Point out cells.
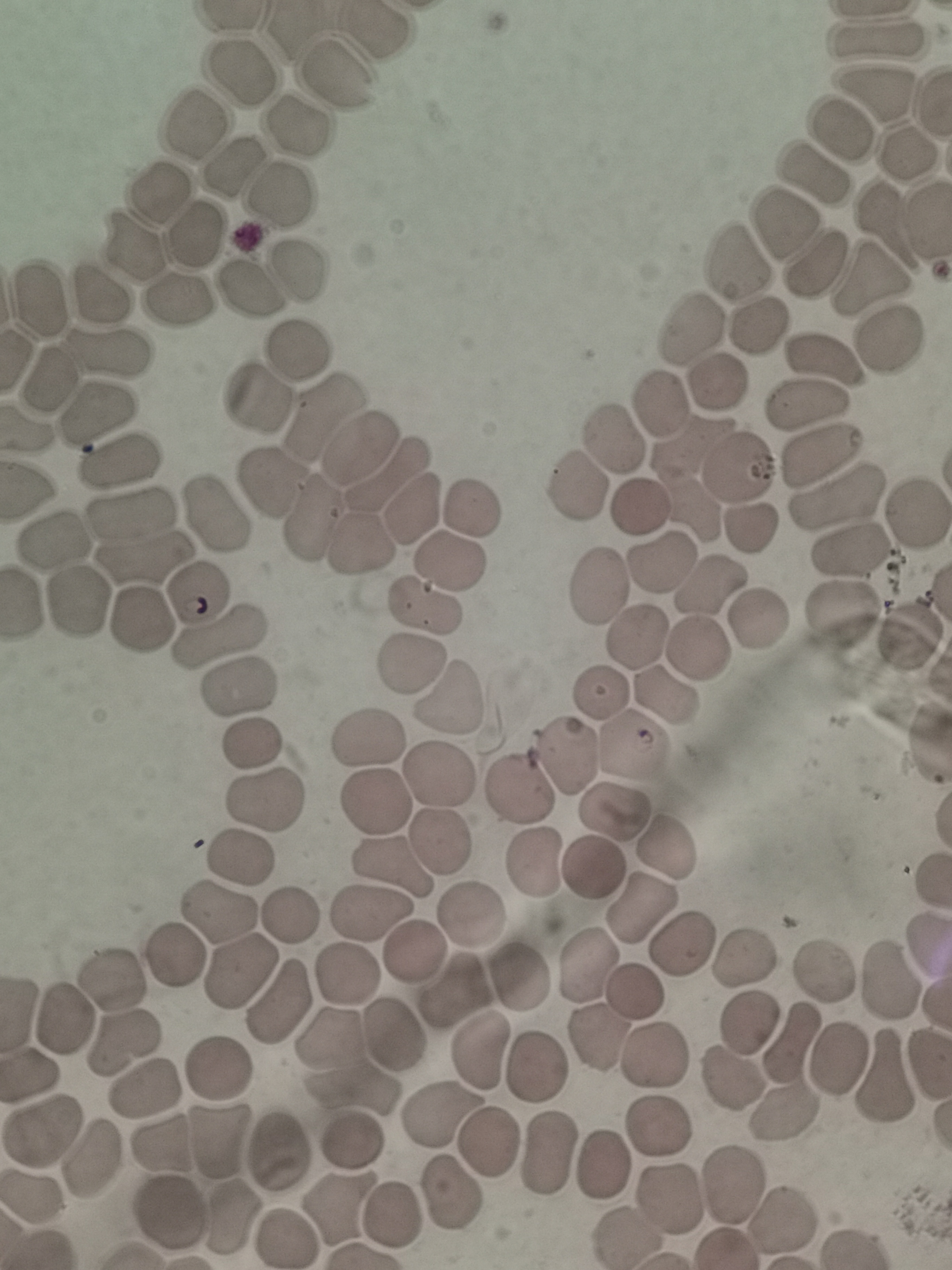

Approximate object centers, in pixels from the top-left corner.
Cells: (x=875, y=37), (x=237, y=70), (x=332, y=74), (x=875, y=94), (x=194, y=125), (x=294, y=125), (x=836, y=131), (x=909, y=151), (x=230, y=167), (x=812, y=172), (x=157, y=189), (x=279, y=193), (x=781, y=226), (x=194, y=234), (x=131, y=246), (x=738, y=260), (x=816, y=263), (x=297, y=270), (x=872, y=276), (x=247, y=289), (x=101, y=293), (x=177, y=299), (x=42, y=300), (x=759, y=325), (x=690, y=331), (x=890, y=339), (x=106, y=349), (x=295, y=354), (x=826, y=356), (x=716, y=380), (x=49, y=381), (x=259, y=395), (x=656, y=400), (x=808, y=402), (x=93, y=414), (x=323, y=416), (x=617, y=440), (x=358, y=449), (x=820, y=453), (x=119, y=463), (x=739, y=468), (x=390, y=477), (x=690, y=479), (x=580, y=483), (x=270, y=485), (x=837, y=492), (x=641, y=503), (x=468, y=508), (x=131, y=510), (x=412, y=510), (x=915, y=513), (x=212, y=515), (x=313, y=519), (x=747, y=526), (x=54, y=541), (x=360, y=547), (x=856, y=551), (x=142, y=558), (x=452, y=560), (x=660, y=562), (x=711, y=584), (x=601, y=586), (x=196, y=593), (x=75, y=599), (x=841, y=606), (x=425, y=607), (x=758, y=619), (x=138, y=624), (x=906, y=636), (x=219, y=637), (x=637, y=639), (x=697, y=648), (x=414, y=664), (x=240, y=685), (x=601, y=691), (x=665, y=694), (x=450, y=696), (x=252, y=738), (x=368, y=739), (x=632, y=743), (x=565, y=751), (x=437, y=768), (x=517, y=788), (x=375, y=797), (x=263, y=798), (x=615, y=809), (x=435, y=839), (x=667, y=845), (x=236, y=856), (x=387, y=860), (x=533, y=862), (x=593, y=869), (x=641, y=906), (x=369, y=912), (x=475, y=913), (x=218, y=915), (x=285, y=916), (x=683, y=941), (x=412, y=949), (x=171, y=955), (x=741, y=960), (x=588, y=965), (x=240, y=971), (x=822, y=975), (x=344, y=976), (x=523, y=980), (x=886, y=983), (x=112, y=985), (x=452, y=992), (x=636, y=996), (x=278, y=1004), (x=64, y=1021), (x=749, y=1024), (x=394, y=1035), (x=327, y=1037), (x=599, y=1037), (x=123, y=1041), (x=788, y=1044), (x=481, y=1050), (x=656, y=1059), (x=838, y=1060), (x=530, y=1068), (x=216, y=1069), (x=880, y=1079), (x=731, y=1080), (x=144, y=1087), (x=349, y=1089), (x=782, y=1112), (x=439, y=1118), (x=659, y=1129), (x=44, y=1136), (x=217, y=1140), (x=166, y=1143), (x=356, y=1143), (x=488, y=1144), (x=546, y=1155), (x=276, y=1156), (x=96, y=1160), (x=602, y=1164), (x=736, y=1182), (x=455, y=1195), (x=31, y=1198), (x=666, y=1202), (x=337, y=1206), (x=394, y=1211), (x=230, y=1216), (x=172, y=1217), (x=780, y=1222), (x=620, y=1237), (x=283, y=1238).

Giemsa stain. Thin blood film. Image is 952×1270 pixels. One field from this slide. Photographed with a smartphone camera at the microscope eyepiece.